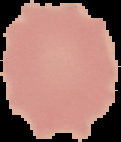
{
  "image_size": "121×142 pixels",
  "malaria_status": "uninfected",
  "image_type": "cell region segmented out of the field of view; surrounding area masked to black",
  "preparation": "thin blood smear"
}